Describe the morphology of the red blood cells.
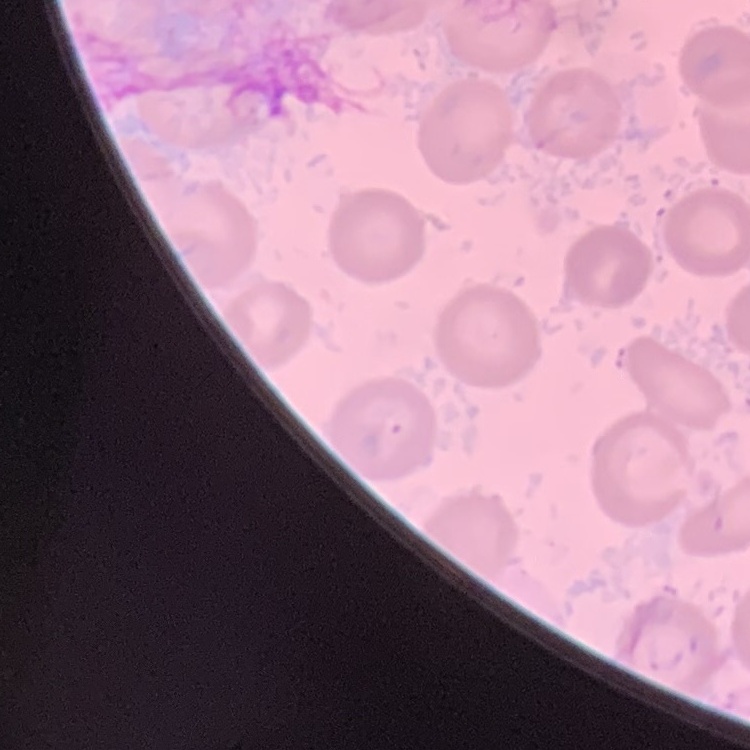
They show no rouleaux formation.

{
  "image_type": "square crop of a larger photomicrograph",
  "stain": "Field's or Giemsa",
  "preparation": "thin peripheral smear"
}